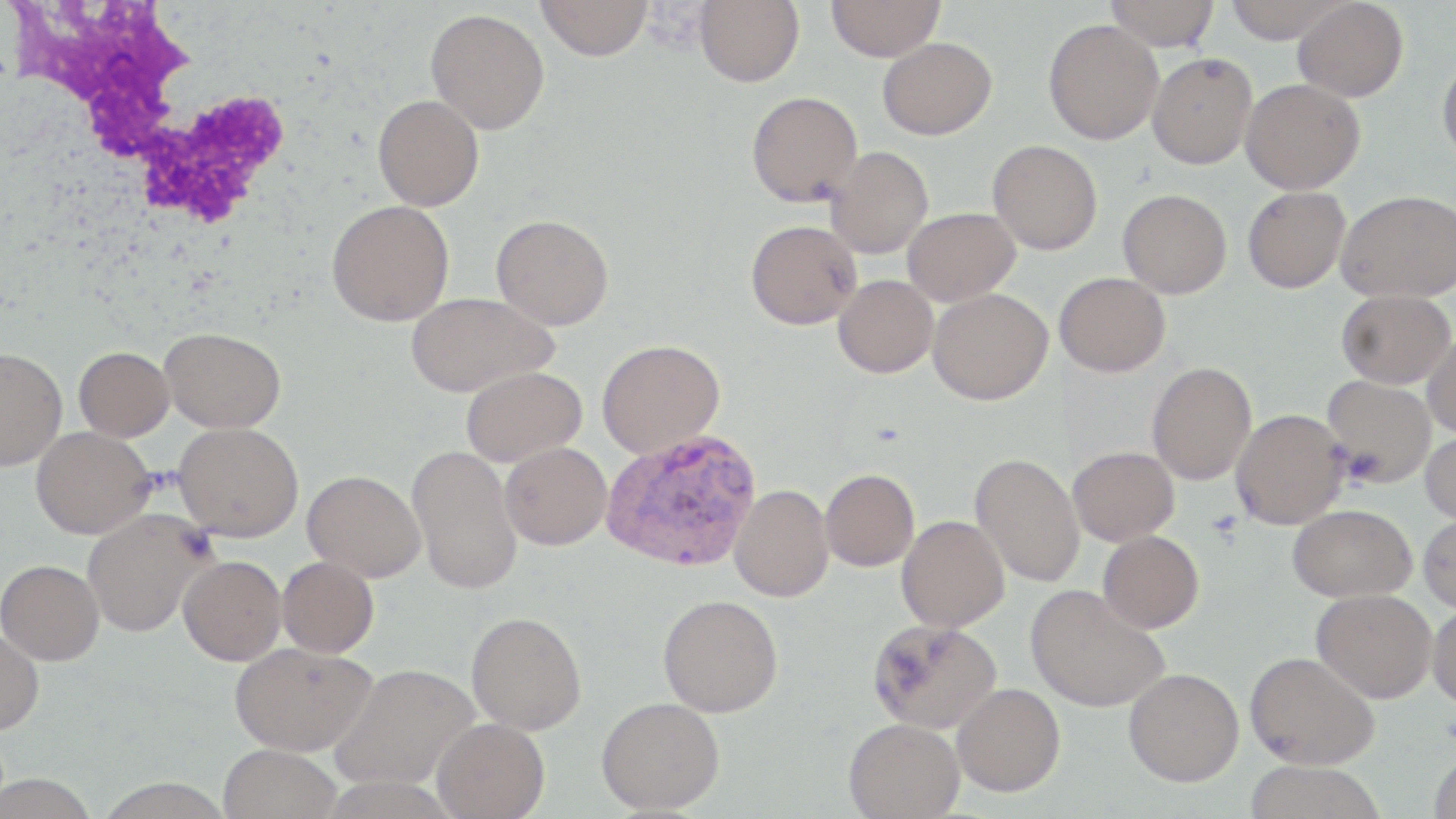

Summary:
  - Coordinate format: approximate bounding boxes as [x1, y1, x2, y2] in pixels
  - Plasmodium vivax-infected red blood cell locations: [599, 428, 761, 573]
  - Uninfected red blood cell locations: [535, 0, 653, 60], [694, 0, 804, 87], [826, 0, 946, 61], [1105, 0, 1220, 51], [1223, 0, 1351, 43], [1292, 0, 1408, 102], [425, 8, 550, 134], [1043, 18, 1163, 145], [877, 37, 997, 139], [1147, 52, 1258, 170], [1437, 54, 1456, 165], [1240, 78, 1365, 194], [746, 91, 863, 207], [372, 94, 484, 210], [987, 140, 1102, 255], [827, 146, 933, 259], [1242, 186, 1350, 293], [1118, 189, 1232, 298], [1336, 189, 1456, 302], [326, 200, 454, 327], [902, 207, 1020, 305], [491, 214, 614, 330], [745, 219, 862, 329], [1054, 272, 1170, 377], [833, 275, 938, 378], [927, 288, 1052, 405], [1337, 289, 1455, 389], [405, 291, 557, 397], [160, 327, 286, 432], [1422, 331, 1456, 440], [597, 339, 726, 459], [74, 346, 174, 441], [0, 347, 67, 471], [1146, 361, 1257, 485], [460, 366, 587, 466], [1321, 376, 1436, 489], [1230, 408, 1350, 529], [174, 421, 303, 542], [31, 426, 156, 539], [1420, 428, 1456, 524], [500, 442, 612, 550], [407, 445, 523, 595], [1067, 446, 1180, 546], [970, 452, 1085, 588], [820, 468, 919, 571], [302, 469, 426, 582], [729, 484, 834, 602], [1287, 504, 1416, 602], [81, 507, 214, 637], [1417, 513, 1456, 612], [896, 515, 1009, 632], [1098, 531, 1204, 633], [177, 555, 287, 666], [276, 555, 379, 658], [0, 559, 104, 665], [1025, 584, 1170, 712], [1311, 589, 1437, 703], [658, 594, 783, 717], [1428, 602, 1456, 710], [466, 611, 587, 735], [867, 618, 1003, 734], [0, 628, 44, 735], [230, 641, 377, 755], [1244, 651, 1380, 770], [329, 661, 480, 790], [1123, 668, 1244, 786], [951, 682, 1065, 796], [596, 696, 725, 814], [432, 717, 550, 819], [844, 717, 965, 818], [218, 744, 342, 819], [1428, 752, 1456, 818], [1242, 760, 1387, 819]
  - White blood cell locations: [4, 1, 298, 236]
  - Slide-level diagnosis: Plasmodium vivax
  - Image size: 1456×819 pixels
  - Stain: May-Grünwald-Giemsa
  - Field of view: single
  - Preparation: thin blood smear
  - Modality: optical microscopy
  - Magnification: 1000x